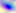
Summary:
  - Modality: photomicrograph
  - Magnification: 400x
  - Identification: Toxoplasma gondii